State which parasite is depicted.
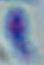
Toxoplasma gondii.

1000x magnification. Micrograph.